Report the malaria status of this cell.
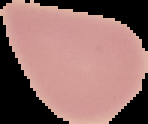

It is uninfected.

Image is 148×124 pixels. Segmented cell region on a black background. From a thin blood film.